Locate every uninfected red blood cell.
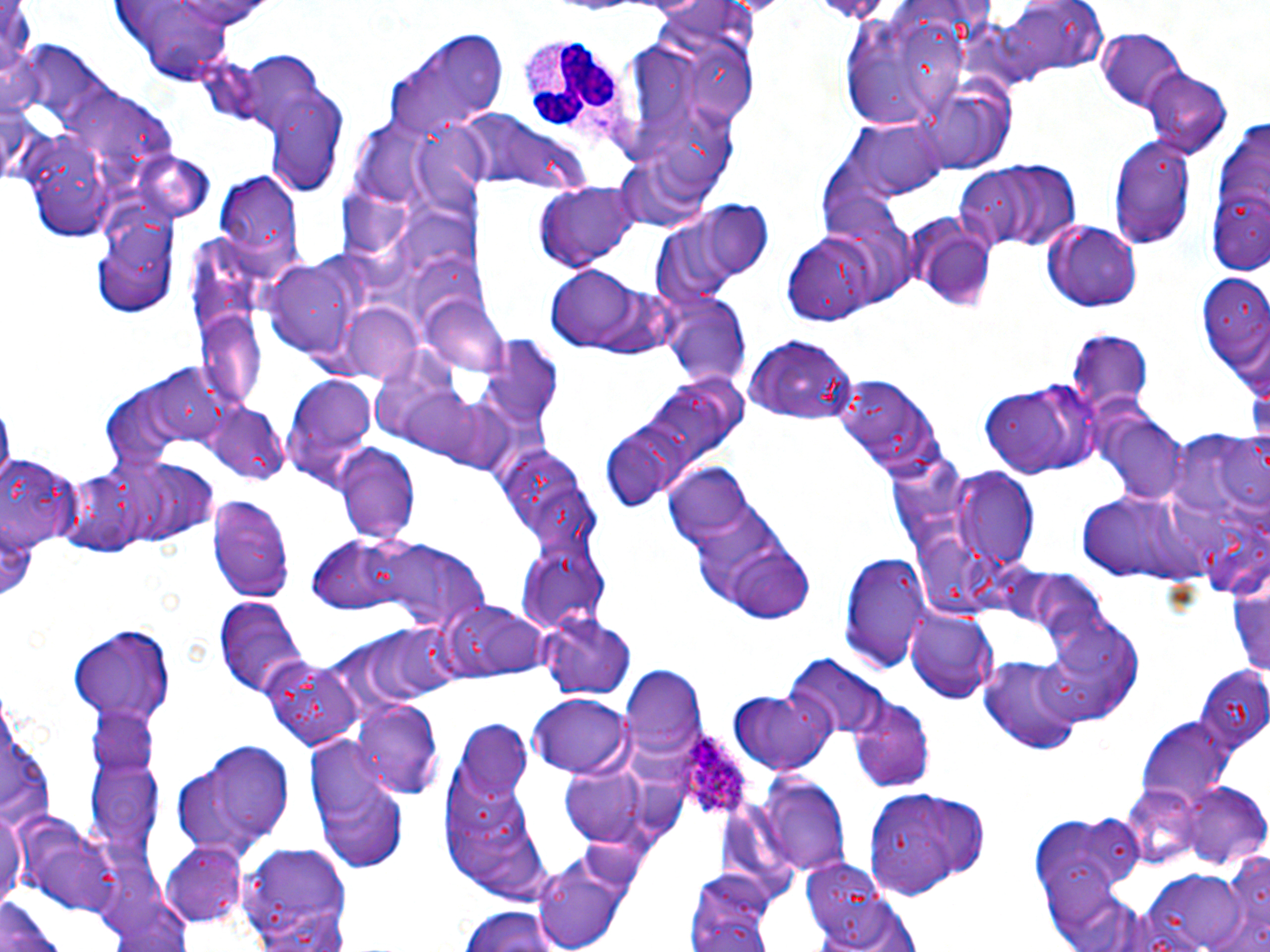
Approximate bounding boxes as (x1,y1)-(x2,y2) corner pairs in pixels.
Uninfected red blood cells: (109,0)-(250,81), (979,4)-(1109,85), (385,27)-(511,139), (1097,29)-(1187,110), (1142,70)-(1230,157), (265,87)-(348,198), (465,114)-(567,189), (850,121)-(944,195), (347,123)-(438,211), (410,124)-(493,206), (1109,135)-(1197,248), (959,163)-(1082,253), (212,167)-(306,280), (535,189)-(640,271), (695,203)-(776,279), (651,208)-(757,304), (908,218)-(994,307), (1045,222)-(1142,310), (782,230)-(878,327), (264,259)-(361,358), (543,264)-(671,358), (1197,276)-(1270,378), (660,289)-(751,392), (423,298)-(515,376), (341,302)-(426,382), (197,312)-(265,410), (1068,331)-(1154,413), (746,334)-(857,426), (281,377)-(378,492), (980,380)-(1098,479), (394,384)-(499,465), (203,404)-(290,485), (1099,411)-(1186,499), (598,426)-(685,511), (334,443)-(420,543), (122,459)-(214,544), (663,464)-(754,546), (954,471)-(1038,565), (207,492)-(295,606), (1075,492)-(1200,581), (308,537)-(412,616), (376,539)-(487,631), (718,540)-(819,624), (837,551)-(933,674), (1229,575)-(1270,683), (212,597)-(309,699), (452,604)-(548,679), (541,610)-(639,701), (906,610)-(999,704), (1040,620)-(1144,723), (69,624)-(177,726), (360,625)-(459,709), (261,654)-(362,753), (786,655)-(890,740), (981,656)-(1086,755), (620,666)-(704,764), (1195,668)-(1270,749), (729,690)-(837,776), (848,693)-(934,791), (529,694)-(632,776), (1,700)-(55,842), (354,702)-(441,799), (87,706)-(157,779), (1137,719)-(1231,808), (457,721)-(531,799), (307,739)-(405,869), (171,740)-(296,860), (86,751)-(162,857), (558,760)-(654,846), (757,774)-(850,874), (1183,784)-(1270,866), (1124,786)-(1203,866), (864,788)-(988,896), (0,807)-(24,911), (23,818)-(124,917), (231,839)-(359,949), (163,841)-(247,923), (1223,845)-(1270,946), (533,850)-(630,952), (799,853)-(895,941), (687,866)-(776,952), (100,881)-(198,952), (812,896)-(920,952), (1,899)-(69,952), (458,906)-(569,952).

slide-level diagnosis = Plasmodium ovale
stain = May-Grünwald-Giemsa
field of view = one of a larger specimen
white blood cell locations = approximate bounding boxes as (x1,y1)-(x2,y2) corner pairs in pixels: (517,33)-(643,161)
image size = 1270×952 pixels
Plasmodium ovale-infected red blood cell locations = approximate bounding boxes as (x1,y1)-(x2,y2) corner pairs in pixels: (664,728)-(759,823)
magnification = 1000x
modality = optical microscopy
preparation = thin blood film